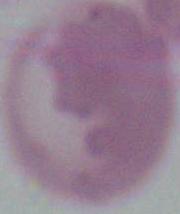

A red blood cell is shown. Captured at 1000x magnification. Photomicrograph.